Name the cell type shown.
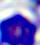

This is a leukocyte.

Summary:
  - Modality: photomicrograph
  - Magnification: 400x